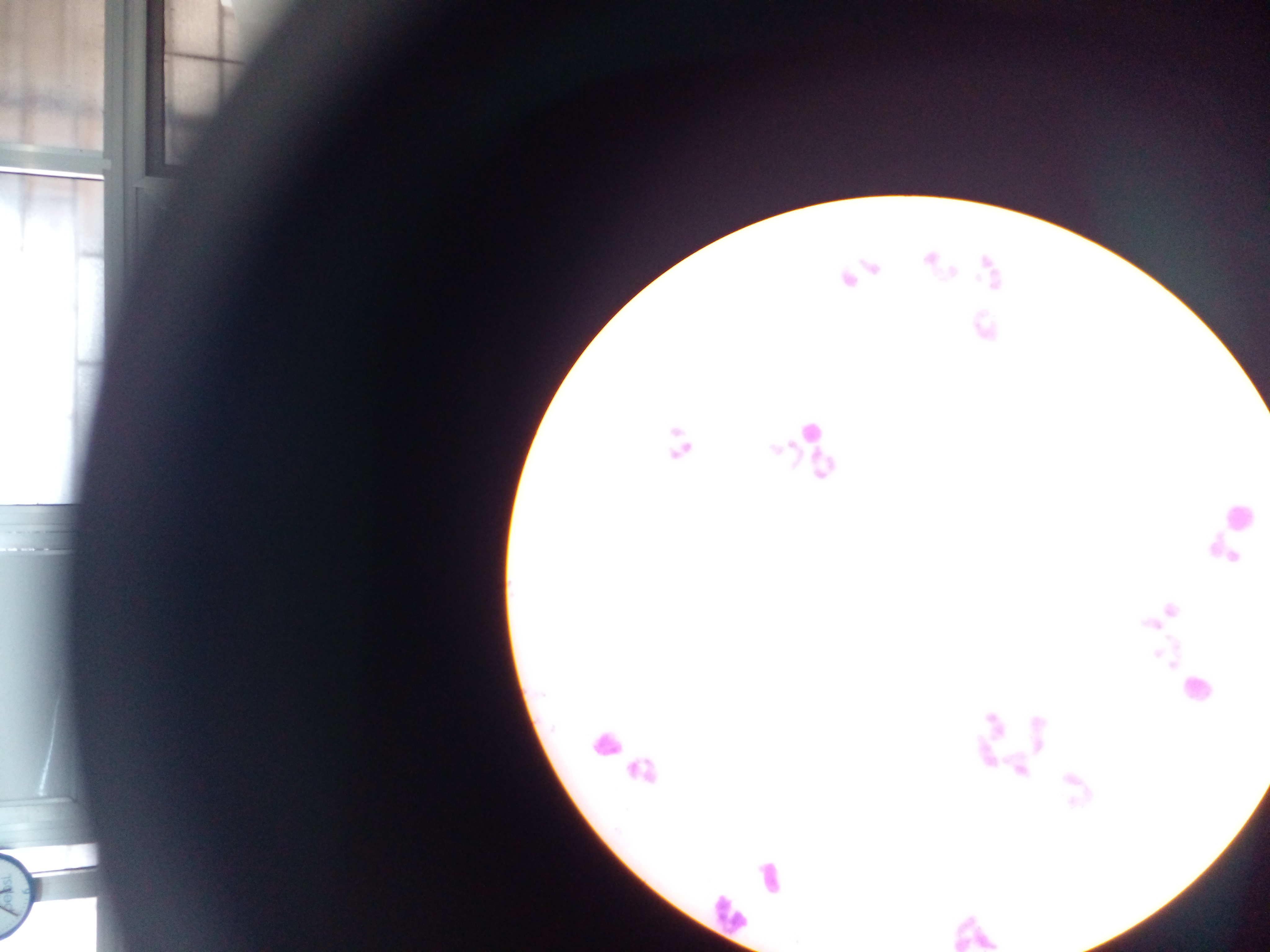

preparation: thick blood smear
country: Ghana
leukocyte_locations: 'approximate centers as [x, y] in pixels: [807, 430], [1234, 518], [1191, 701], [611, 746], [637, 771], [778, 871], [726, 917]'
image_size: 1270×952 pixels
field_of_view: single
capture: mobile-phone photograph through a microscope